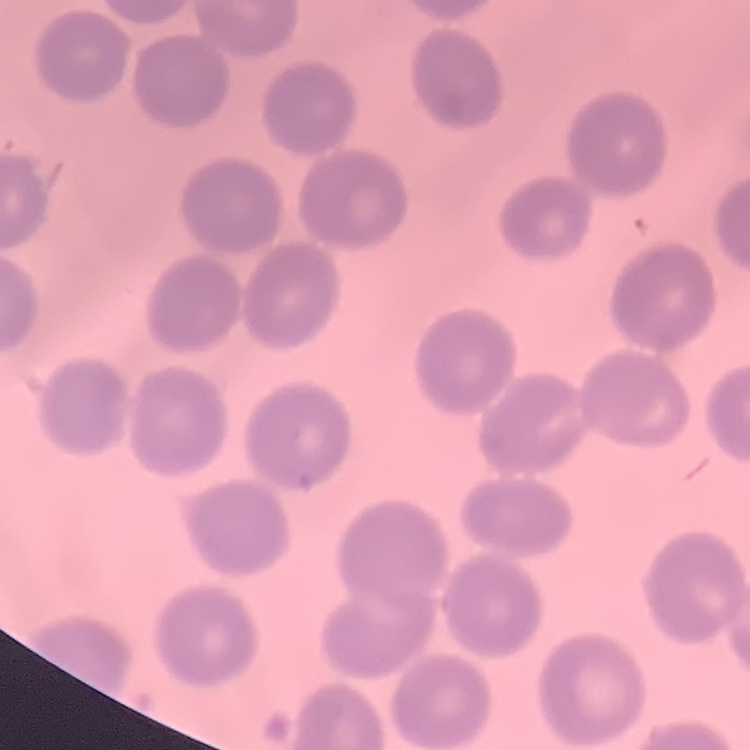
The erythrocytes show no rouleaux formation. Stained with either Field's or Giemsa. Thin peripheral smear. Square crop of a larger photomicrograph.